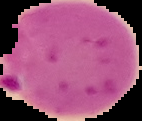
Result: malaria parasites detected. Image is 142×121 pixels. The area outside the segmented cell region is set to black. From a thin blood smear.